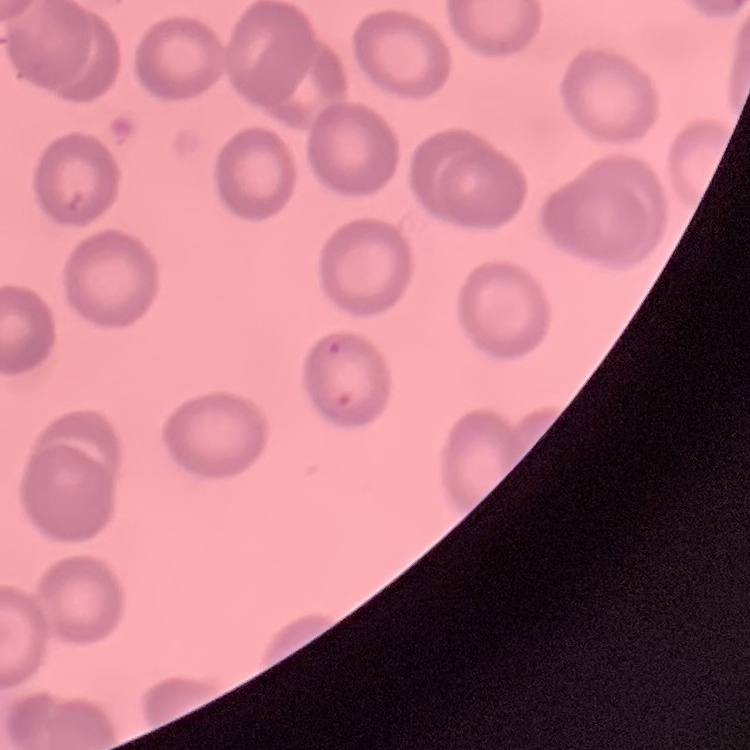
Summary:
  - Erythrocyte morphology: no rouleaux formation
  - Stain: Field's or Giemsa
  - Image type: one tile cut from a larger photomicrograph
  - Preparation: thin peripheral smear